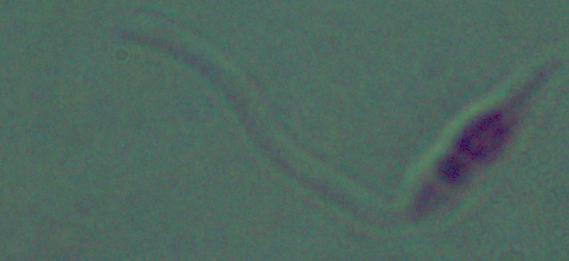
Summary:
  - Magnification: 1000x
  - Modality: micrograph
  - Identification: Leishmania